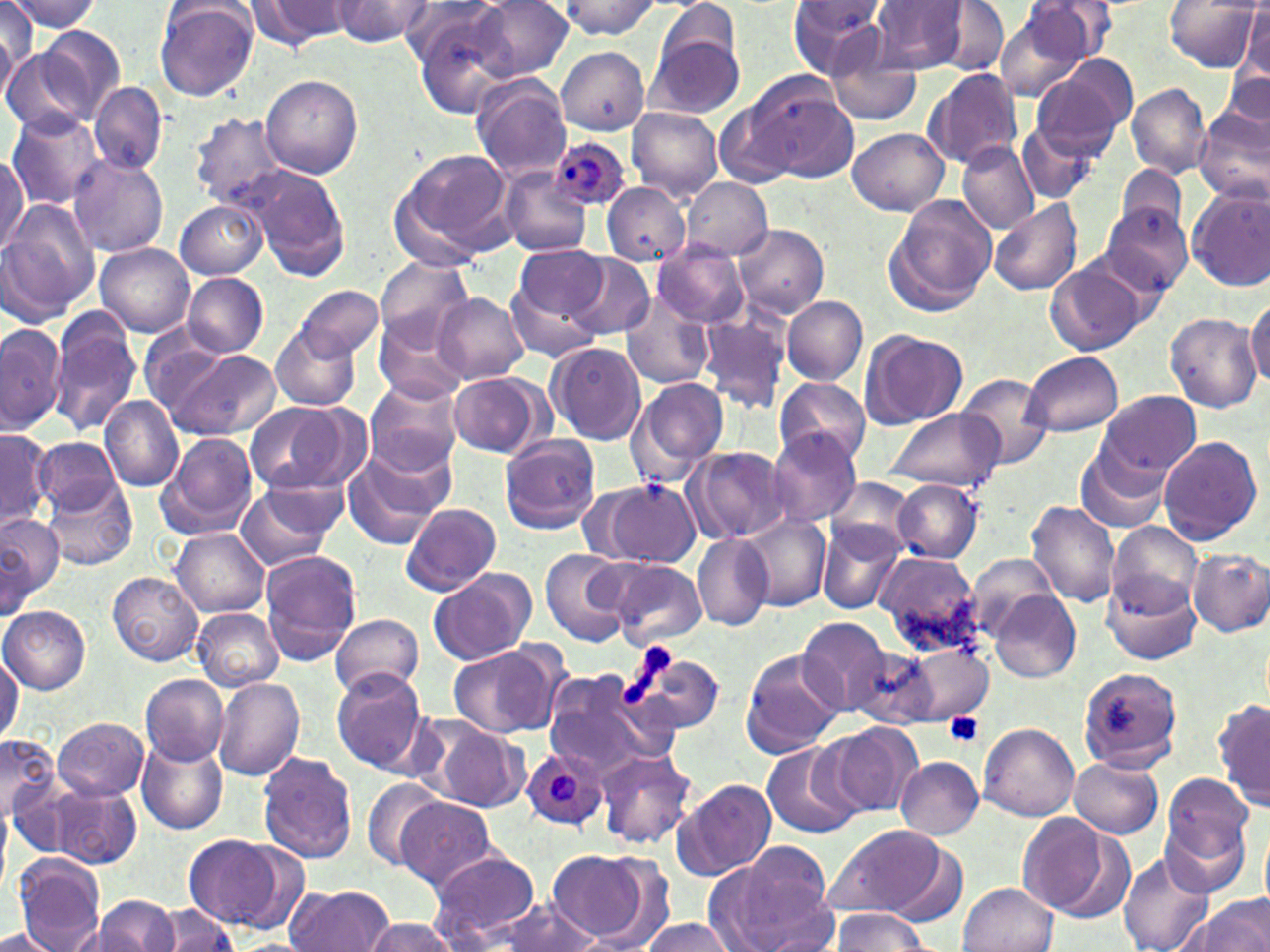

slide-level diagnosis = Plasmodium ovale
image size = 1270×952 pixels
modality = light microscopy
field of view = single
uninfected red blood cell locations = approximate bounding boxes as [x1, y1, x2, y2] in pixels: [0, 0, 38, 77], [6, 0, 103, 33], [245, 0, 352, 48], [333, 0, 434, 45], [405, 0, 511, 103], [788, 0, 887, 79], [871, 0, 969, 75], [1023, 0, 1117, 67], [470, 1, 572, 82], [559, 1, 661, 38], [655, 1, 740, 73], [1166, 1, 1262, 71], [154, 2, 259, 103], [937, 2, 1009, 75], [1241, 5, 1269, 81], [0, 9, 21, 99], [994, 10, 1084, 102], [36, 26, 127, 122], [648, 31, 745, 119], [825, 36, 924, 126], [3, 45, 99, 138], [554, 46, 650, 134], [1058, 55, 1138, 134], [922, 67, 1024, 171], [1032, 71, 1130, 160], [1221, 72, 1270, 136], [735, 73, 860, 184], [261, 75, 363, 180], [472, 77, 572, 181], [89, 82, 167, 175], [1127, 83, 1212, 179], [627, 105, 722, 201], [1195, 106, 1270, 204], [8, 111, 105, 212], [190, 113, 290, 209], [1015, 120, 1099, 202], [847, 127, 949, 215], [957, 141, 1037, 233], [391, 149, 514, 262], [0, 153, 29, 253], [69, 156, 169, 259], [1114, 163, 1191, 242], [247, 168, 352, 280], [499, 168, 593, 259], [680, 178, 772, 261], [603, 183, 690, 265], [1187, 186, 1270, 290], [886, 195, 996, 313], [988, 199, 1083, 295], [176, 200, 267, 279], [1, 203, 99, 320], [1102, 205, 1193, 295], [734, 223, 830, 319], [95, 243, 196, 337], [652, 243, 748, 327], [516, 244, 607, 321], [564, 253, 655, 341], [375, 256, 473, 347], [1045, 260, 1151, 354], [183, 273, 269, 357], [503, 279, 602, 364], [296, 284, 383, 362], [433, 293, 529, 385], [621, 293, 714, 390], [1246, 295, 1270, 388], [781, 297, 868, 384], [47, 308, 142, 439], [696, 311, 792, 414], [1166, 311, 1261, 413], [376, 313, 471, 405], [0, 322, 65, 432], [271, 325, 360, 412], [861, 329, 968, 430], [547, 342, 646, 445], [160, 347, 281, 441], [1023, 351, 1122, 435], [956, 372, 1054, 469], [448, 373, 545, 457], [364, 377, 463, 477], [630, 377, 730, 482], [775, 377, 869, 469], [1098, 390, 1202, 479], [99, 397, 182, 492], [244, 401, 362, 496], [887, 408, 1003, 492], [0, 431, 51, 531], [767, 431, 862, 525], [156, 433, 258, 540], [500, 435, 602, 534], [1157, 435, 1264, 545], [35, 437, 119, 515], [1074, 441, 1173, 534], [341, 446, 450, 548], [684, 447, 792, 545], [41, 475, 136, 571], [828, 476, 918, 559], [892, 480, 983, 562], [605, 481, 700, 566], [234, 484, 341, 571], [1026, 500, 1121, 606], [399, 503, 501, 597], [1, 513, 63, 608], [739, 513, 831, 610], [818, 522, 906, 613], [1106, 522, 1203, 615], [170, 528, 270, 617], [691, 533, 774, 630], [539, 548, 630, 646], [1187, 549, 1270, 636], [874, 550, 984, 652], [259, 551, 361, 664], [968, 553, 1063, 639], [604, 559, 707, 648], [427, 568, 537, 666], [108, 571, 202, 665], [1104, 574, 1202, 665], [990, 590, 1080, 683], [1, 607, 89, 693], [193, 609, 284, 691], [330, 614, 423, 701], [797, 617, 894, 715], [448, 643, 566, 739], [903, 644, 993, 725], [619, 645, 725, 736], [850, 645, 940, 730], [739, 649, 845, 759], [0, 655, 20, 745], [1078, 665, 1183, 775], [539, 668, 675, 779], [330, 670, 434, 776], [140, 674, 228, 766], [212, 676, 306, 781], [1215, 698, 1270, 812], [412, 715, 530, 811], [54, 717, 149, 800], [978, 721, 1079, 820], [823, 723, 924, 819], [1, 734, 59, 821], [137, 738, 228, 834], [761, 743, 862, 842], [594, 750, 697, 849], [258, 752, 357, 865], [897, 756, 983, 838], [1069, 758, 1164, 838], [1159, 774, 1255, 890], [671, 777, 778, 881], [360, 778, 447, 873], [45, 784, 142, 869], [396, 797, 498, 892], [1017, 813, 1121, 918], [1260, 820, 1270, 911], [821, 824, 955, 920], [182, 833, 290, 926], [708, 846, 838, 952], [1118, 848, 1213, 952], [548, 850, 656, 945], [426, 851, 541, 946], [14, 856, 105, 952], [959, 882, 1056, 952], [287, 884, 394, 952], [91, 895, 177, 952], [1190, 896, 1270, 951], [487, 899, 599, 951], [151, 905, 239, 952], [831, 909, 931, 950], [362, 916, 457, 952], [636, 917, 736, 951], [0, 927, 60, 951]
stain = May-Grünwald-Giemsa
platelet locations = approximate bounding boxes as [x1, y1, x2, y2] in pixels: [638, 642, 672, 676], [617, 674, 655, 710], [944, 713, 984, 748]
Plasmodium ovale-infected red blood cell locations = approximate bounding boxes as [x1, y1, x2, y2] in pixels: [552, 136, 629, 208], [520, 745, 608, 833]
magnification = 1000x
preparation = thin blood smear